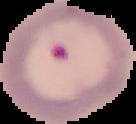
Cell region segmented out of the field of view; the surrounding area is masked to black. Image is 136×124 pixels. From a thin blood film. Result: Plasmodium parasites identified.